State which cell type is depicted.
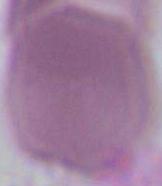

This is an erythrocyte.

Summary:
  - Magnification: 1000x
  - Modality: photomicrograph